Assess this cell for malaria.
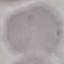
It is uninfected.

Thin blood smear. Photographed with a smartphone camera at the microscope eyepiece. Cell patch, automatically extracted from a larger field of view and resized to 64 × 64 pixels. Giemsa-stained preparation.